Report the malaria status of this cell.
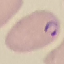

Parasitized.

Giemsa-stained preparation. Thin blood smear. Acquired by smartphone through the microscope eyepiece. Automatically extracted cell patch, resized to 64 × 64 pixels.